Name the parasite shown.
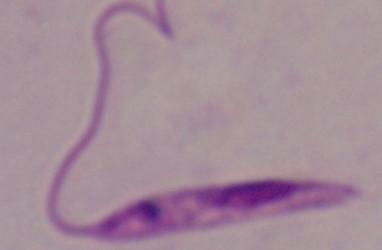

Leishmania.

Summary:
  - Modality: photomicrograph
  - Magnification: 1000x